Assess this cell for malaria.
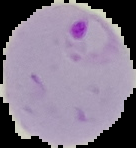

It is parasitized.

From a thin blood smear. Image is 136×148 pixels. Cell region segmented out of the field of view; the surrounding area is masked to black.